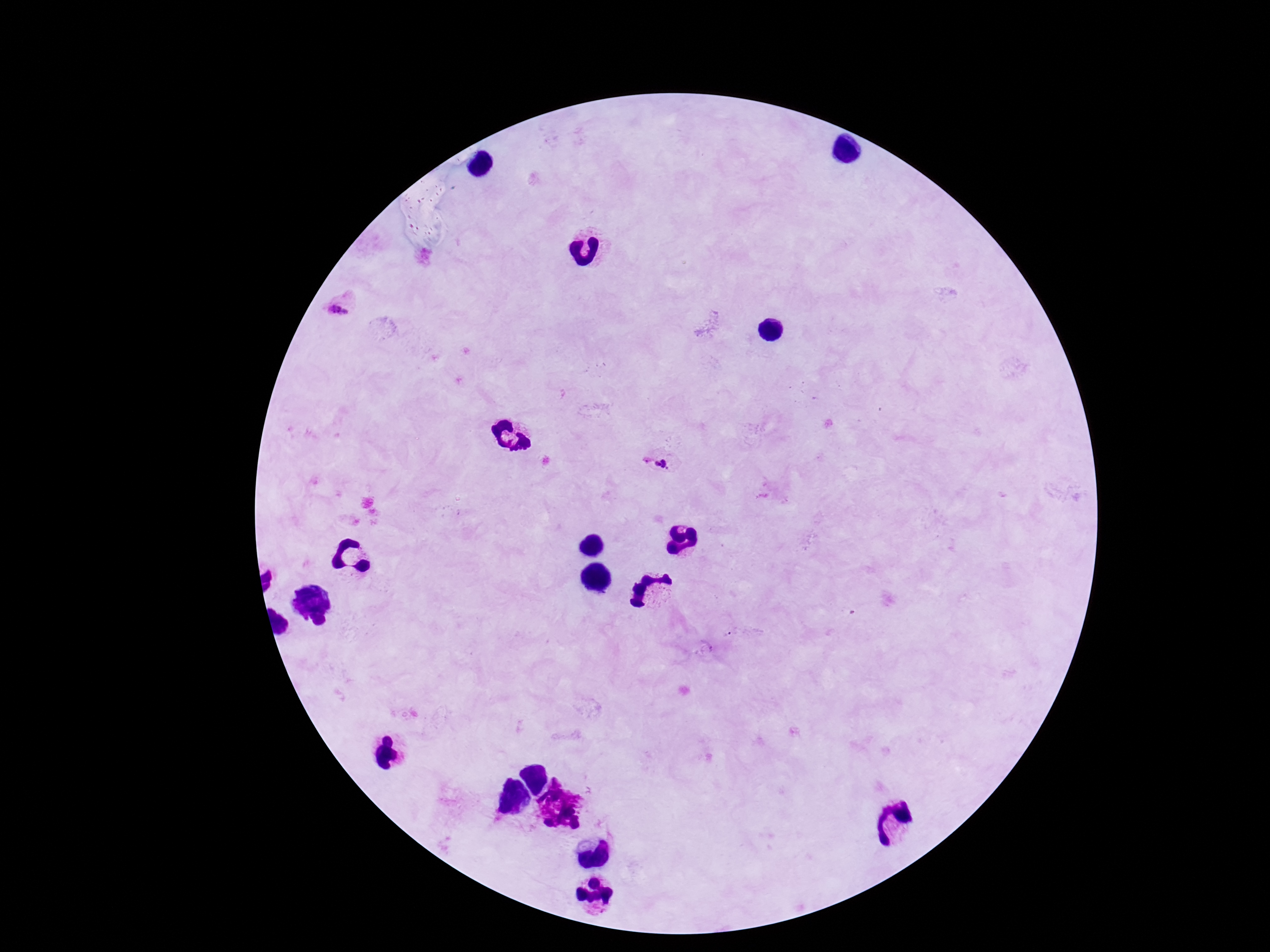 Approximate object centers, in pixels from the top-left corner. Plasmodium parasite locations: (x=660, y=461). Thick blood smear. Single field of view. Image is 1270×952 pixels. Giemsa-stained preparation. 100x magnification. Patient malaria status: positive. Photographed through the microscope eyepiece with a smartphone camera.